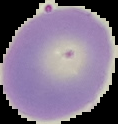
Summary:
  - Preparation: thin blood smear
  - Malaria status: uninfected
  - Image size: 118×124 pixels
  - Image type: segmented cell region with the area outside set to black